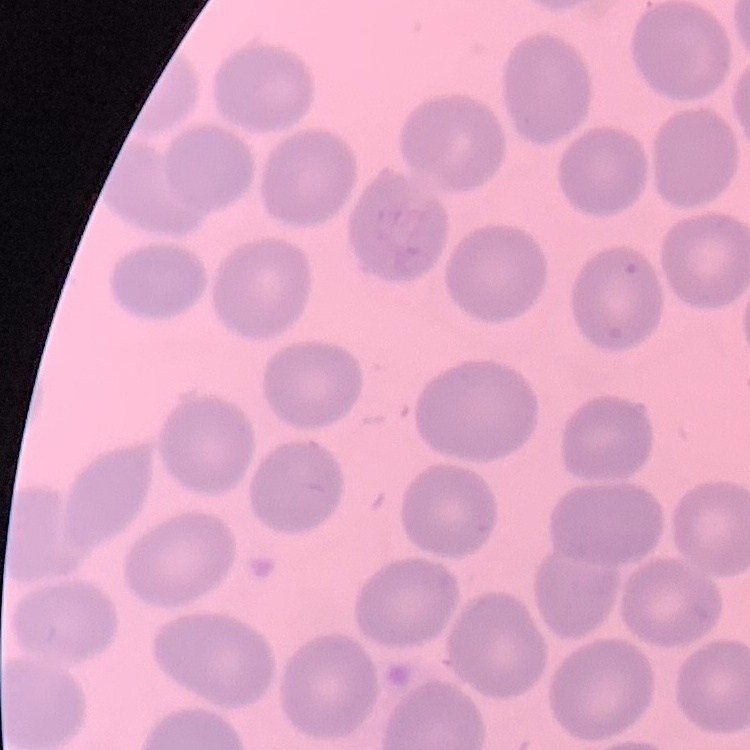
{
  "erythrocyte_morphology": "no rouleaux formation",
  "image_type": "one tile cut from a larger photomicrograph",
  "stain": "Field's or Giemsa",
  "preparation": "thin peripheral smear"
}